Assess the morphology of the red blood cells.
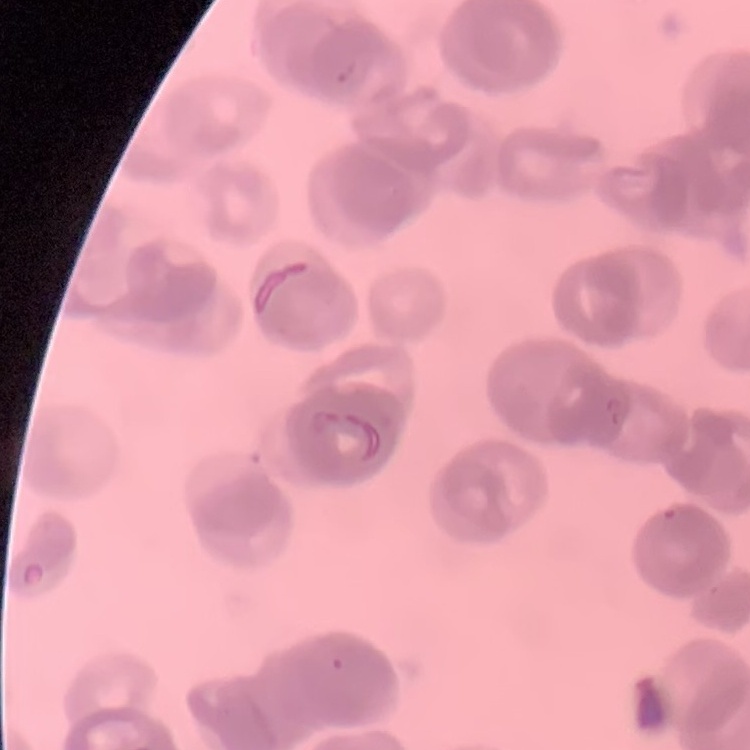
They show rouleaux formation.

Summary:
  - Stain: Field's or Giemsa
  - Image type: one tile cut from a larger photomicrograph
  - Preparation: thin blood film